Assess the morphology of the erythrocytes.
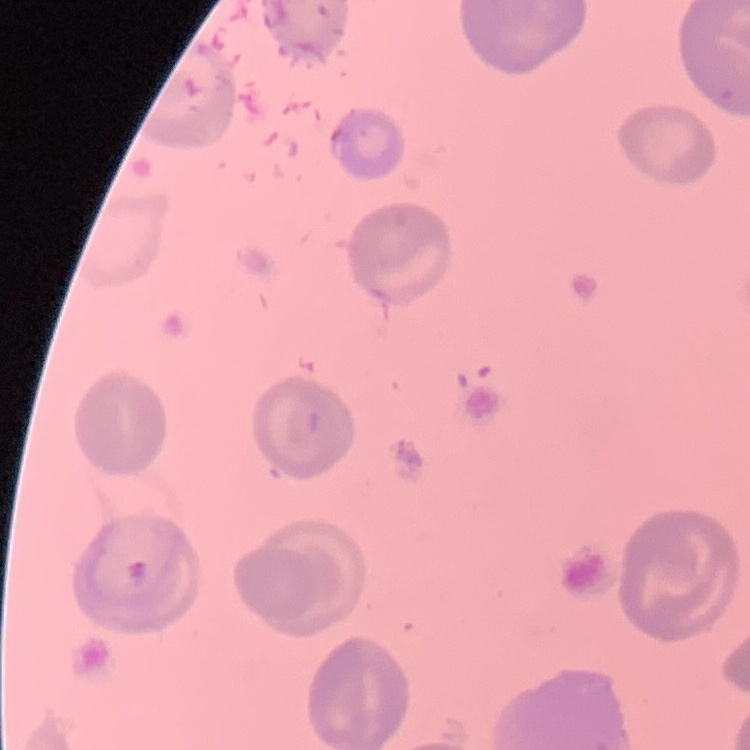

No rouleaux formation.

One tile cut from a larger photomicrograph. Stained with either Field's or Giemsa. Thin blood smear.